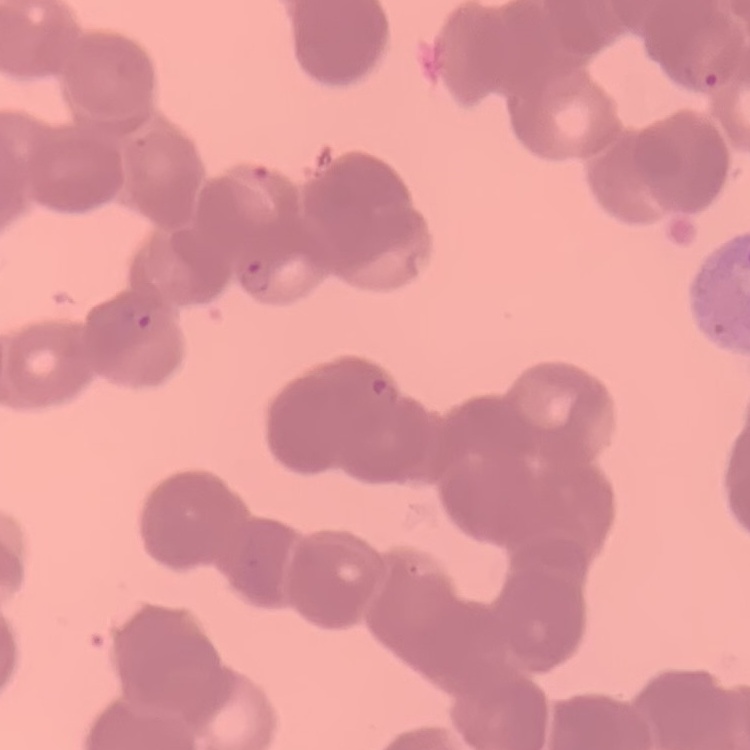

erythrocyte morphology = rouleaux formation
stain = Field's or Giemsa
image type = square crop of a larger photomicrograph
preparation = thin blood smear